Identify the parasite.
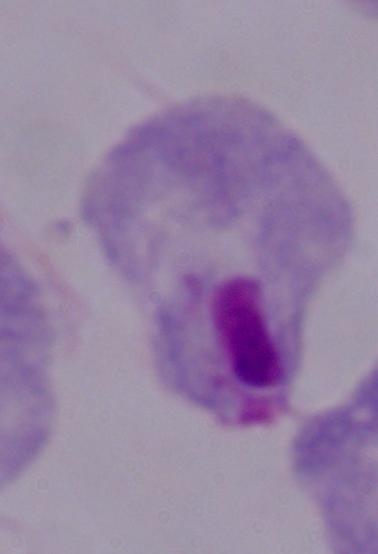

A trichomonad.

Summary:
  - Modality: photomicrograph
  - Magnification: 1000x